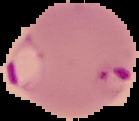 From a thin blood film. Image is 139×121 pixels. Result: Plasmodium parasites identified. Segmented cell region on a black background.